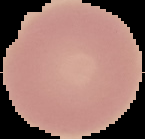

image type = segmented cell region with the area outside set to black
image size = 145×139 pixels
preparation = thin blood film
result = no Plasmodium parasites seen